Locate every Plasmodium parasite and every leukocyte.
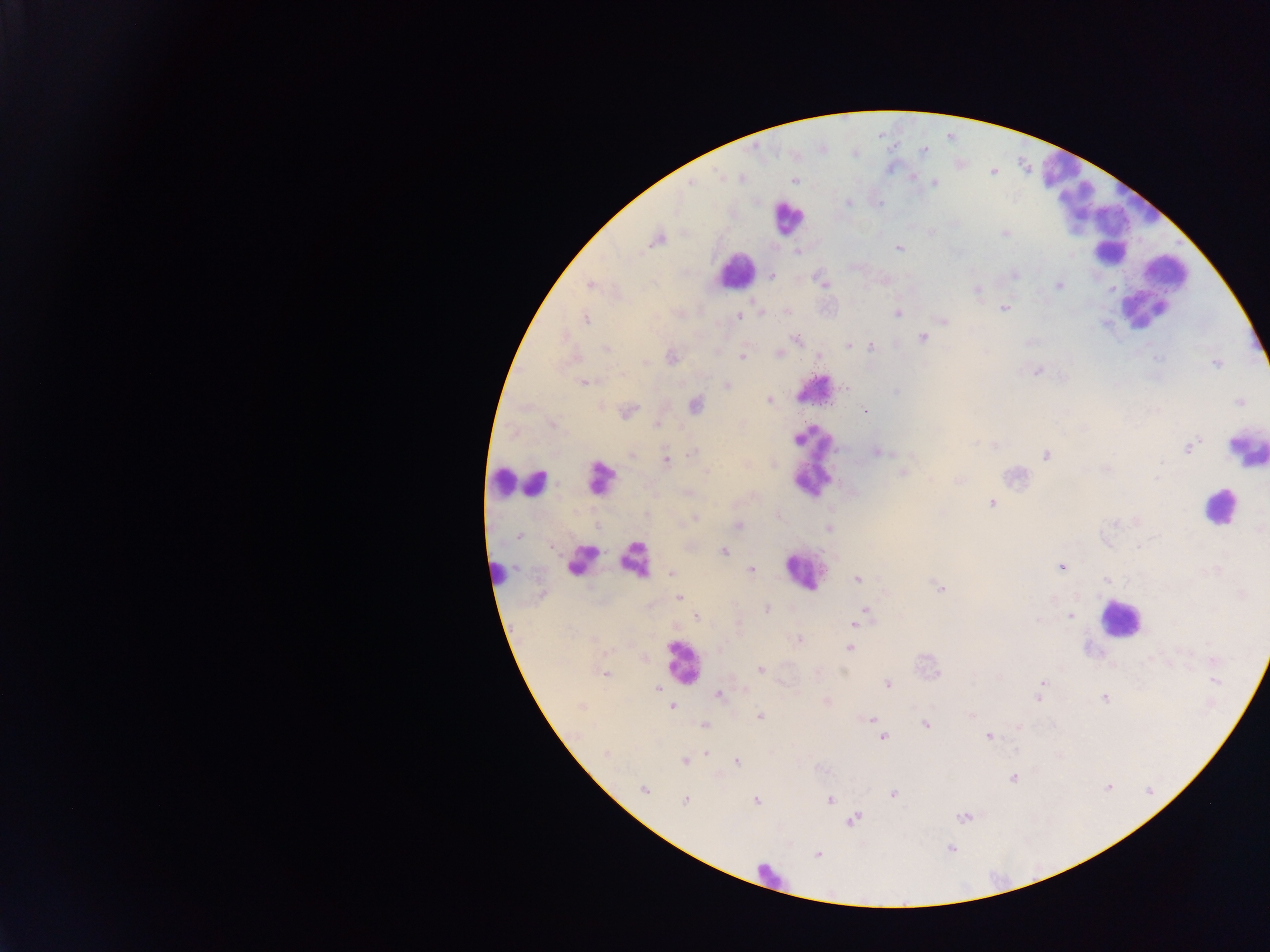
Approximate centers as {x, y} in pixels.
Plasmodium parasites: {923, 151}, {741, 178}, {913, 178}, {691, 181}, {794, 181}, {934, 183}, {847, 203}, {1005, 233}, {657, 239}, {898, 248}, {796, 251}, {1014, 274}, {771, 275}, {883, 279}, {823, 282}, {589, 284}, {1059, 285}, {977, 290}, {1004, 308}, {760, 312}, {787, 312}, {897, 313}, {739, 315}, {585, 318}, {942, 319}, {922, 337}, {796, 338}, {847, 344}, {870, 347}, {607, 348}, {779, 354}, {818, 355}, {742, 356}, {672, 357}, {574, 358}, {1217, 364}, {1037, 370}, {584, 382}, {727, 385}, {769, 400}, {1240, 402}, {695, 405}, {627, 411}, {865, 411}, {552, 424}, {655, 424}, {1187, 447}, {876, 452}, {692, 453}, {631, 455}, {1046, 455}, {666, 460}, {902, 472}, {958, 480}, {687, 492}, {992, 502}, {695, 518}, {738, 525}, {828, 527}, {1259, 529}, {518, 535}, {724, 551}, {1061, 566}, {751, 569}, {670, 572}, {857, 579}, {1106, 580}, {940, 589}, {677, 597}, {765, 609}, {866, 610}, {696, 615}, {1068, 615}, {854, 624}, {798, 640}, {850, 648}, {644, 657}, {760, 670}, {604, 673}, {887, 684}, {1042, 685}, {657, 688}, {718, 694}, {1038, 696}, {1105, 697}, {826, 702}, {671, 706}, {971, 715}, {759, 717}, {871, 719}, {876, 723}, {925, 724}, {704, 725}, {1019, 727}, {988, 735}, {883, 736}, {705, 753}, {684, 760}, {736, 761}, {1012, 778}, {1107, 787}, {644, 790}, {892, 794}, {684, 800}, {756, 800}, {829, 800}, {964, 816}, {852, 819}, {950, 847}, {817, 854}.
Leukocytes: {1059, 170}, {1075, 202}, {1141, 202}, {787, 217}, {1111, 249}, {735, 271}, {1166, 271}, {1143, 309}, {815, 390}, {1246, 448}, {813, 464}, {599, 479}, {535, 481}, {505, 483}, {1220, 506}, {582, 559}, {634, 560}, {803, 571}, {498, 574}, {1119, 618}, {682, 661}, {769, 875}.

Summary:
  - Country: Ghana
  - Capture: mobile-phone photograph through a microscope
  - Field of view: single
  - Image size: 1270×952 pixels
  - Preparation: thick blood smear